Describe the morphology of the red blood cells.
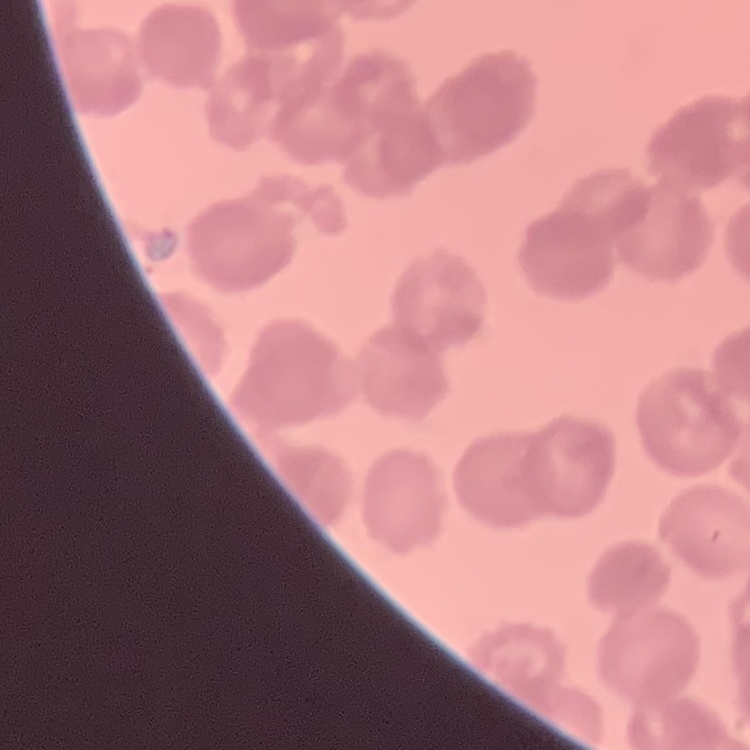
Rouleaux formation.

Summary:
  - Image type: square crop of a larger photomicrograph
  - Preparation: thin blood film
  - Stain: Field's or Giemsa